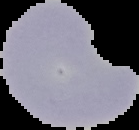 Segmented cell region on a black background. Malaria status: parasitized. From a thin blood film. Image is 139×130 pixels.